Report the malaria status of this cell.
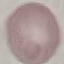
It is uninfected.

Summary:
  - Stain: Giemsa
  - Image type: cell patch, automatically extracted from a larger field of view and resized to 64 × 64 pixels
  - Preparation: thin smear
  - Capture: smartphone camera at the microscope eyepiece